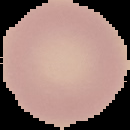
Summary:
  - Preparation: thin blood film
  - Result: negative for malaria parasites
  - Image size: 130×130 pixels
  - Image type: segmented cell region with the area outside set to black